Report the malaria status of this cell.
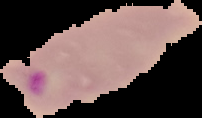
It is parasitized.

From a thin blood smear. Cell region segmented out of the field of view; the surrounding area is masked to black. Image is 202×118 pixels.